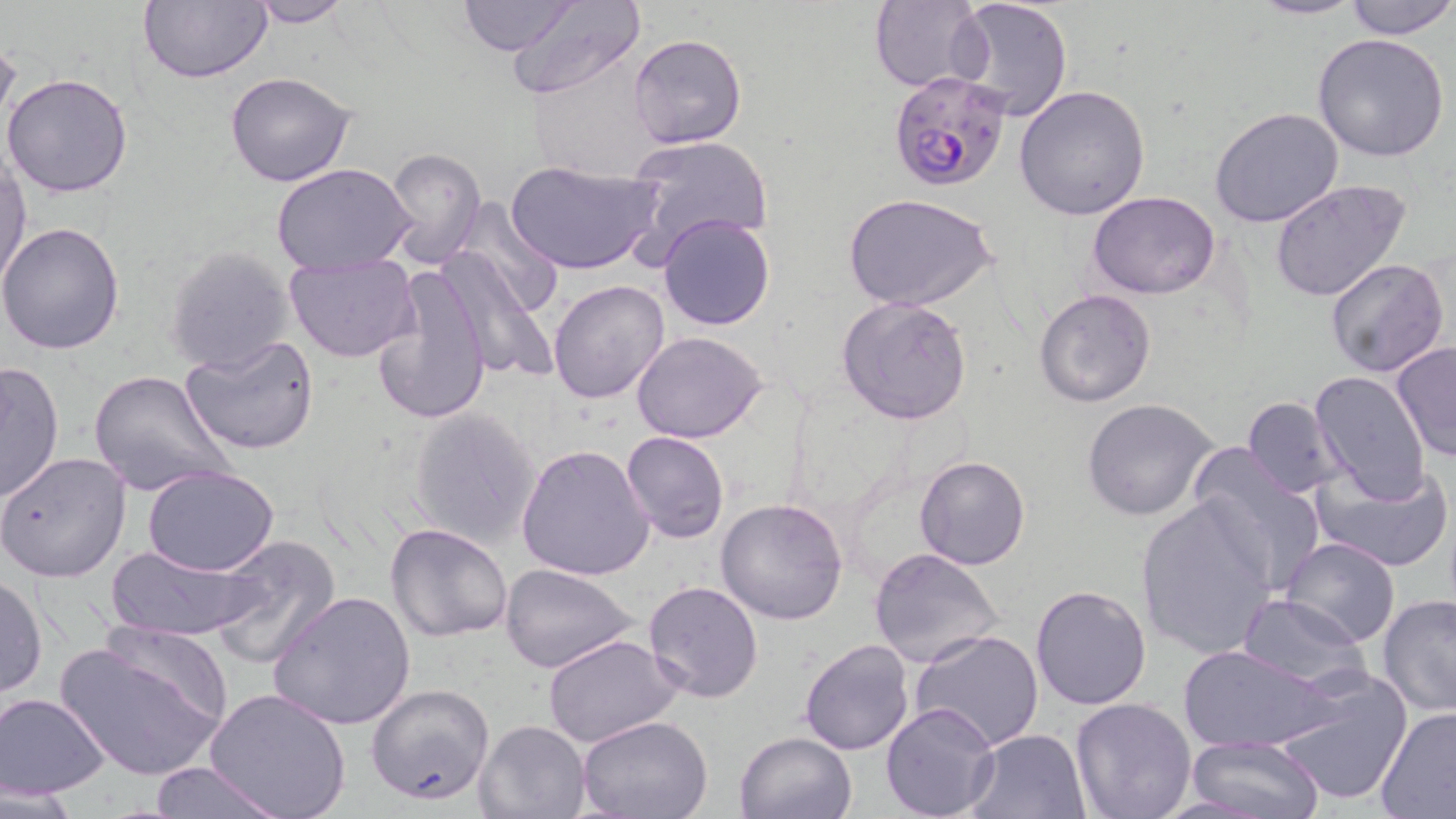
Summary:
  - Coordinate format: approximate bounding boxes as named x1/y1/x2/y2 corners in pixels
  - Uninfected red blood cell locations: (x1=139, y1=0, x2=271, y2=83), (x1=456, y1=0, x2=581, y2=55), (x1=946, y1=0, x2=1074, y2=122), (x1=1250, y1=0, x2=1364, y2=20), (x1=1344, y1=0, x2=1455, y2=40), (x1=242, y1=1, x2=357, y2=27), (x1=504, y1=1, x2=646, y2=101), (x1=869, y1=1, x2=988, y2=91), (x1=0, y1=29, x2=22, y2=140), (x1=627, y1=33, x2=747, y2=151), (x1=1311, y1=33, x2=1451, y2=163), (x1=528, y1=59, x2=668, y2=187), (x1=3, y1=72, x2=134, y2=197), (x1=225, y1=72, x2=359, y2=187), (x1=1014, y1=83, x2=1151, y2=221), (x1=1210, y1=107, x2=1344, y2=228), (x1=625, y1=133, x2=776, y2=263), (x1=383, y1=146, x2=486, y2=268), (x1=0, y1=151, x2=31, y2=293), (x1=503, y1=161, x2=664, y2=278), (x1=273, y1=165, x2=415, y2=276), (x1=1268, y1=179, x2=1412, y2=304), (x1=1087, y1=190, x2=1220, y2=298), (x1=846, y1=194, x2=997, y2=313), (x1=448, y1=196, x2=566, y2=320), (x1=658, y1=213, x2=776, y2=332), (x1=0, y1=222, x2=126, y2=355), (x1=434, y1=246, x2=553, y2=381), (x1=164, y1=247, x2=297, y2=374), (x1=285, y1=252, x2=418, y2=361), (x1=1324, y1=257, x2=1451, y2=377), (x1=372, y1=265, x2=491, y2=427), (x1=549, y1=280, x2=671, y2=405), (x1=1033, y1=288, x2=1157, y2=408), (x1=836, y1=297, x2=973, y2=425), (x1=631, y1=330, x2=769, y2=442), (x1=180, y1=336, x2=319, y2=456), (x1=1390, y1=340, x2=1456, y2=464), (x1=0, y1=360, x2=64, y2=504), (x1=89, y1=371, x2=234, y2=500), (x1=1308, y1=371, x2=1433, y2=504), (x1=1242, y1=396, x2=1347, y2=497), (x1=1082, y1=397, x2=1220, y2=521), (x1=407, y1=408, x2=541, y2=548), (x1=621, y1=431, x2=729, y2=542), (x1=515, y1=442, x2=657, y2=581), (x1=1184, y1=444, x2=1326, y2=596), (x1=0, y1=451, x2=131, y2=581), (x1=913, y1=454, x2=1031, y2=571), (x1=1310, y1=458, x2=1453, y2=573), (x1=140, y1=465, x2=281, y2=577), (x1=715, y1=496, x2=849, y2=626), (x1=1134, y1=497, x2=1281, y2=660), (x1=384, y1=522, x2=513, y2=643), (x1=204, y1=535, x2=342, y2=669), (x1=1281, y1=536, x2=1401, y2=649), (x1=106, y1=542, x2=266, y2=643), (x1=869, y1=549, x2=1003, y2=669), (x1=500, y1=564, x2=640, y2=675), (x1=1, y1=573, x2=48, y2=699), (x1=643, y1=580, x2=764, y2=702), (x1=1031, y1=584, x2=1152, y2=711), (x1=267, y1=590, x2=416, y2=731), (x1=1235, y1=593, x2=1369, y2=692), (x1=1376, y1=594, x2=1456, y2=719), (x1=909, y1=630, x2=1045, y2=753), (x1=543, y1=634, x2=682, y2=748), (x1=53, y1=638, x2=227, y2=781), (x1=798, y1=638, x2=914, y2=756), (x1=1178, y1=643, x2=1333, y2=752), (x1=1270, y1=667, x2=1414, y2=806), (x1=365, y1=683, x2=495, y2=806), (x1=205, y1=687, x2=350, y2=818), (x1=2, y1=692, x2=110, y2=797), (x1=1069, y1=698, x2=1197, y2=819), (x1=880, y1=701, x2=1001, y2=819), (x1=1374, y1=706, x2=1456, y2=818), (x1=577, y1=715, x2=714, y2=819), (x1=473, y1=719, x2=591, y2=818), (x1=966, y1=729, x2=1091, y2=819), (x1=734, y1=733, x2=857, y2=819), (x1=1185, y1=734, x2=1323, y2=818), (x1=146, y1=762, x2=288, y2=818), (x1=1, y1=784, x2=79, y2=818)
  - Plasmodium falciparum-infected red blood cell locations: (x1=886, y1=69, x2=1011, y2=195)
  - Slide-level diagnosis: Plasmodium falciparum
  - Stain: May-Grünwald-Giemsa
  - Modality: optical microscopy
  - Magnification: 1000x
  - Image size: 1456×819 pixels
  - Preparation: thin blood smear
  - Field of view: single